Identify the cell.
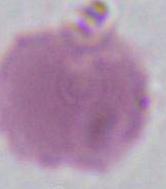

This is an erythrocyte.

magnification: 1000x
modality: photomicrograph